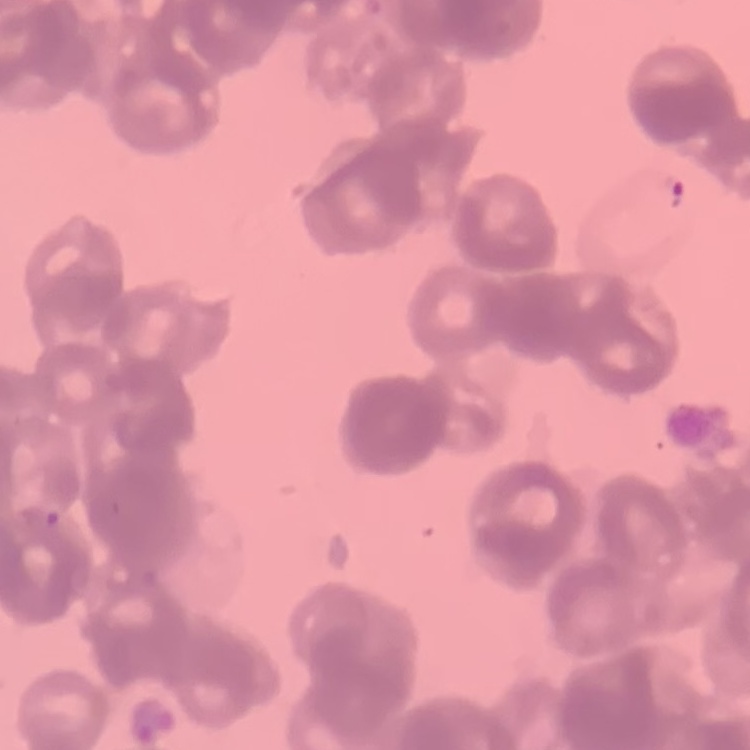
The red blood cells show rouleaux formation. Square crop of a larger photomicrograph. Stained with either Field's or Giemsa. Thin blood smear.